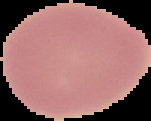

image size = 151×121 pixels
preparation = thin blood smear
image type = cell region segmented out of the field of view; surrounding area masked to black
malaria status = uninfected